Report the malaria status of this cell.
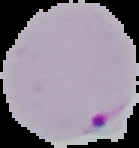
It is parasitized.

Summary:
  - Image size: 139×148 pixels
  - Image type: cell region segmented out of the field of view; surrounding area masked to black
  - Preparation: thin blood film